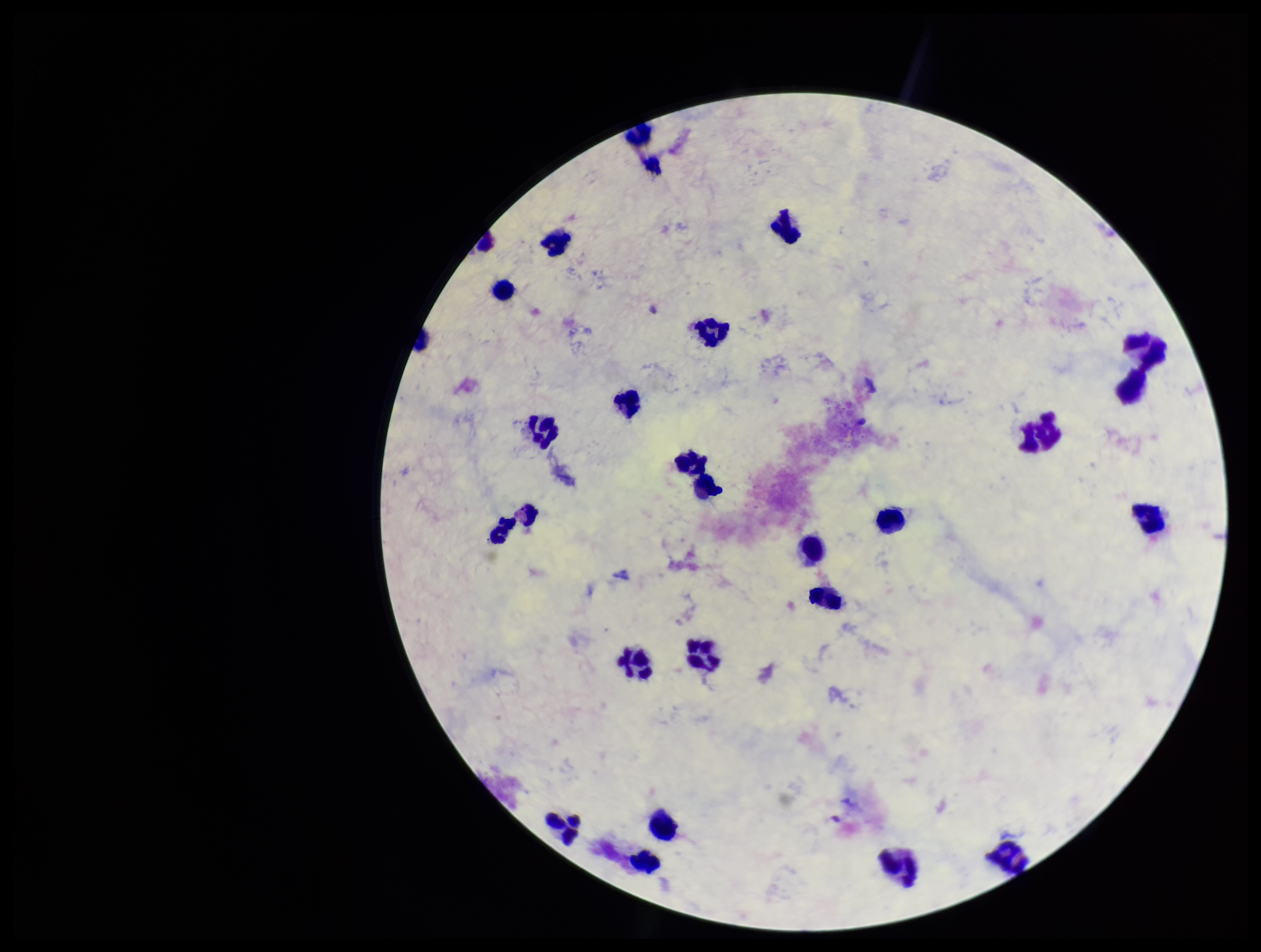 Single field of view. Giemsa stain. Preparation: thick blood smear. Plasmodium parasites: none seen. Patient malaria status: negative. Parasite count: 0. Photographed through the microscope eyepiece with a smartphone camera. Image is 1261×952 pixels. Leukocyte count: 24.